Describe the morphology of the erythrocytes.
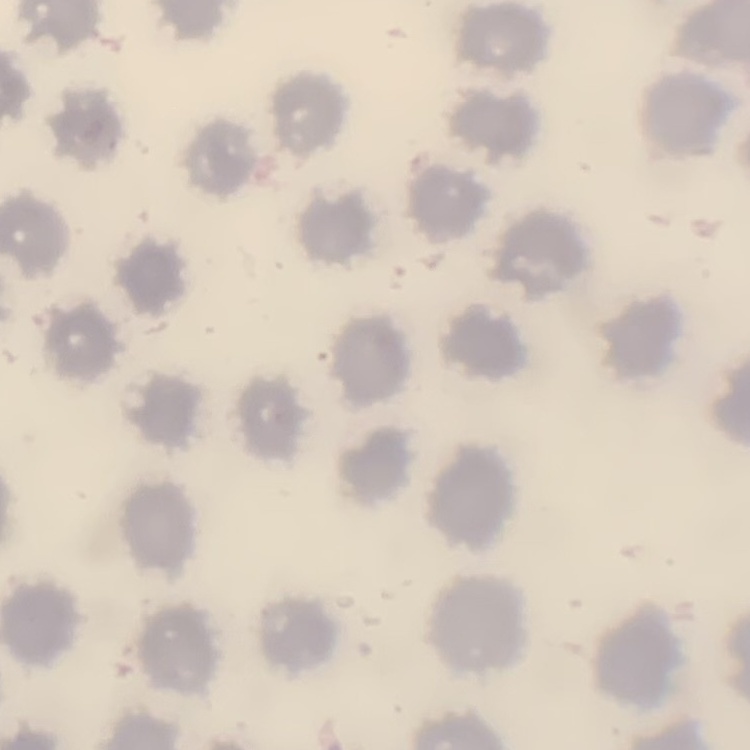

No rouleaux formation.

One tile cut from a larger photomicrograph. Stained with either Field's or Giemsa. Thin peripheral smear.